Assess this cell for malaria.
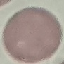
Uninfected.

{
  "stain": "Giemsa",
  "image_type": "automatically extracted cell patch, resized to 64 × 64 pixels",
  "capture": "smartphone through the microscope eyepiece",
  "preparation": "thin smear"
}